Name the parasite shown.
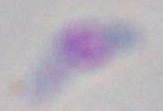
Toxoplasma gondii.

Captured at 1000x magnification. Photomicrograph.